Describe the morphology of the erythrocytes.
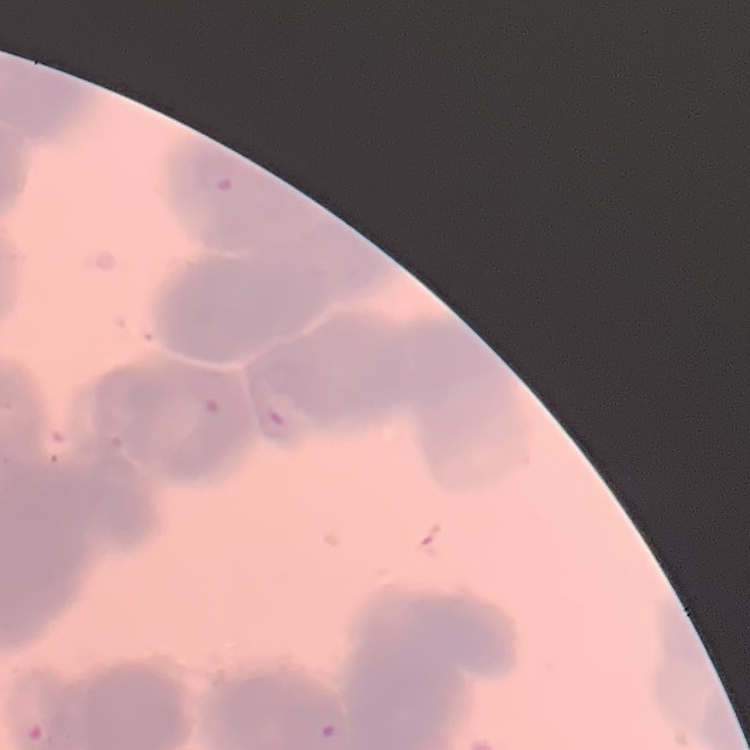

They show rouleaux formation.

Stained with either Field's or Giemsa. One tile cut from a larger photomicrograph. Thin peripheral smear.